Identify the parasite.
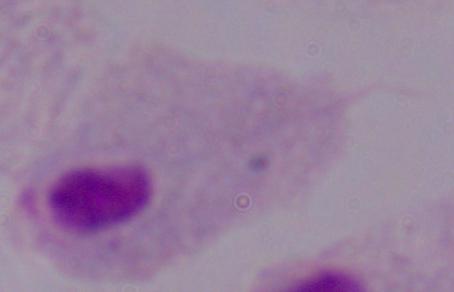
A trichomonad.

magnification = 1000x
modality = photomicrograph